State the blood parasite species.
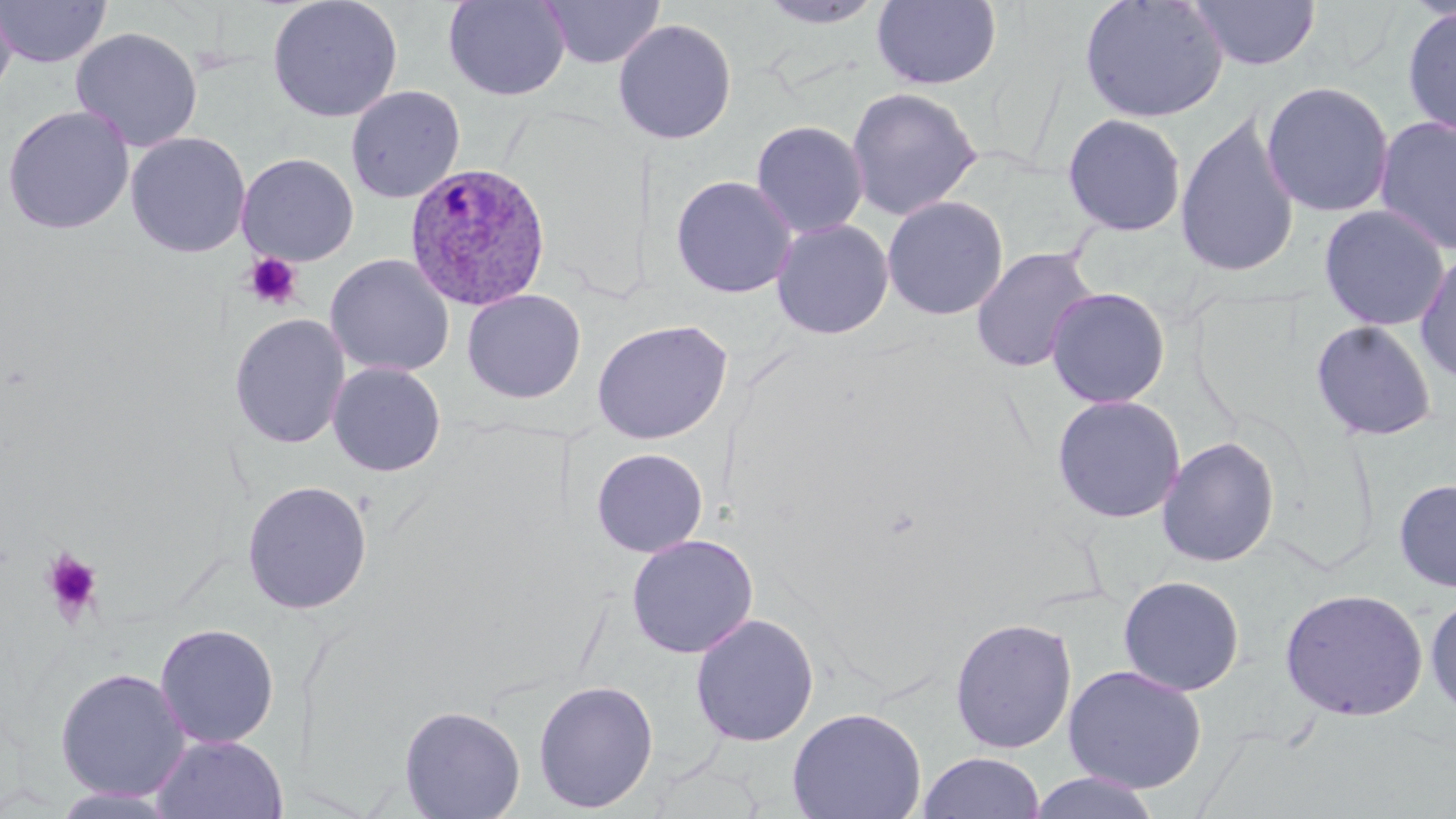
Plasmodium ovale.

Approximate bounding boxes as (x1, y1, x2, y2) in pixels. Plasmodium ovale-infected red blood cell locations: (405, 162, 552, 312). Platelet locations: (242, 252, 303, 311), (42, 549, 103, 622). Uninfected red blood cell locations: (0, 0, 17, 105), (1, 0, 112, 68), (266, 0, 403, 123), (442, 0, 572, 101), (538, 0, 666, 69), (754, 0, 887, 29), (871, 0, 1001, 90), (1078, 0, 1229, 124), (1188, 0, 1321, 71), (1400, 4, 1456, 139), (612, 18, 738, 145), (70, 26, 203, 153), (1260, 80, 1396, 218), (345, 85, 465, 204), (846, 86, 982, 221), (1, 105, 135, 235), (1061, 113, 1188, 237), (1175, 114, 1300, 278), (1374, 114, 1456, 256), (750, 119, 869, 239), (537, 131, 650, 301), (125, 132, 251, 258), (237, 153, 359, 266), (670, 175, 798, 299), (881, 195, 1009, 321), (1318, 204, 1451, 331), (771, 218, 895, 340), (970, 246, 1099, 374), (1414, 248, 1456, 386), (325, 253, 455, 378), (1045, 286, 1171, 409), (461, 288, 586, 404), (229, 313, 351, 449), (591, 318, 733, 445), (1310, 319, 1438, 442), (327, 361, 446, 477), (1051, 394, 1186, 524), (1156, 436, 1281, 568), (591, 447, 709, 558), (1393, 478, 1456, 593), (241, 479, 373, 615), (626, 533, 759, 658), (1118, 575, 1246, 696), (1279, 587, 1429, 722), (1425, 592, 1456, 721), (690, 613, 819, 747), (949, 617, 1078, 754), (154, 623, 280, 748), (1063, 664, 1207, 794), (54, 667, 191, 801), (532, 679, 659, 813), (398, 704, 526, 819), (786, 707, 927, 819), (151, 734, 288, 819), (917, 752, 1045, 818), (1026, 771, 1163, 819). May-Grünwald-Giemsa-stained preparation. Image is 1456×819 pixels. Single field of view. 1000x magnification. Optical microscopy. Thin blood film.